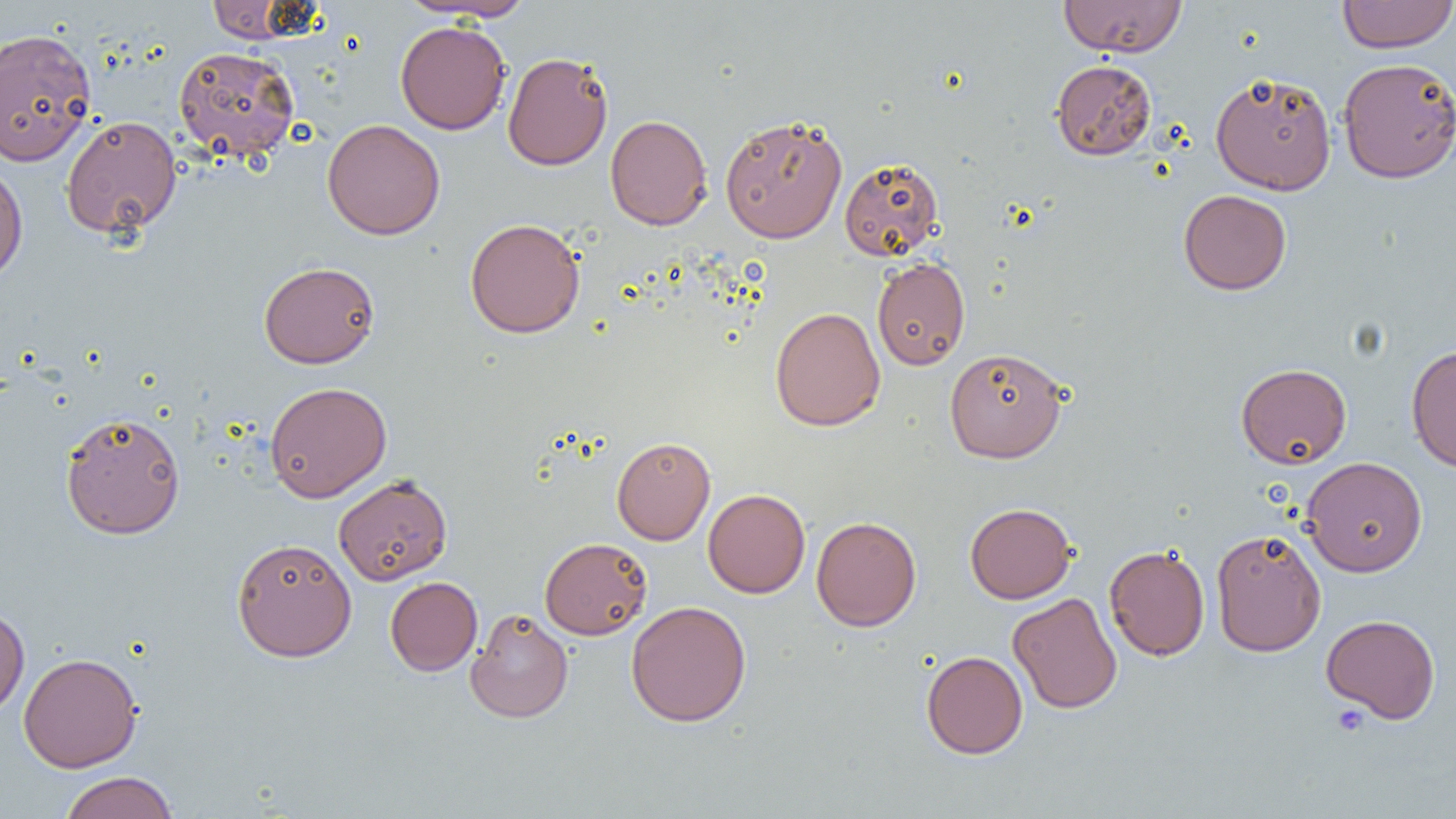 Approximate bounding boxes as (x1, y1, x2, y2) in pixels. Platelet locations: (1331, 704, 1370, 737). Uninfected red blood cell locations: (205, 0, 315, 44), (401, 0, 537, 21), (1058, 0, 1187, 57), (1337, 0, 1455, 53), (395, 20, 510, 134), (0, 28, 97, 166), (173, 46, 300, 161), (502, 51, 613, 170), (1337, 57, 1456, 183), (1051, 60, 1156, 160), (1210, 71, 1337, 195), (605, 114, 712, 230), (720, 114, 847, 243), (61, 116, 182, 239), (322, 119, 445, 240), (839, 157, 944, 261), (0, 160, 28, 285), (1178, 189, 1292, 295), (465, 218, 585, 338), (872, 257, 970, 370), (258, 261, 380, 368), (770, 306, 885, 432), (1406, 344, 1456, 472), (944, 347, 1068, 463), (1236, 363, 1352, 468), (265, 381, 392, 503), (59, 410, 186, 540), (611, 437, 715, 545), (1301, 456, 1428, 576), (333, 474, 452, 585), (703, 489, 810, 598), (965, 503, 1076, 604), (811, 516, 921, 631), (1210, 527, 1326, 656), (231, 537, 357, 661), (539, 537, 652, 640), (1104, 544, 1210, 661), (385, 576, 482, 676), (1007, 592, 1122, 714), (626, 600, 752, 727), (0, 605, 30, 716), (465, 608, 574, 723), (1320, 614, 1441, 723), (921, 650, 1028, 759), (18, 652, 143, 772), (58, 771, 179, 819). Slide-level diagnosis: no evidence of blood parasites. Captured at 1000x magnification. Single field of view. Optical microscopy. Thin blood film. Image is 1456×819 pixels.